Assess the morphology of the red blood cells.
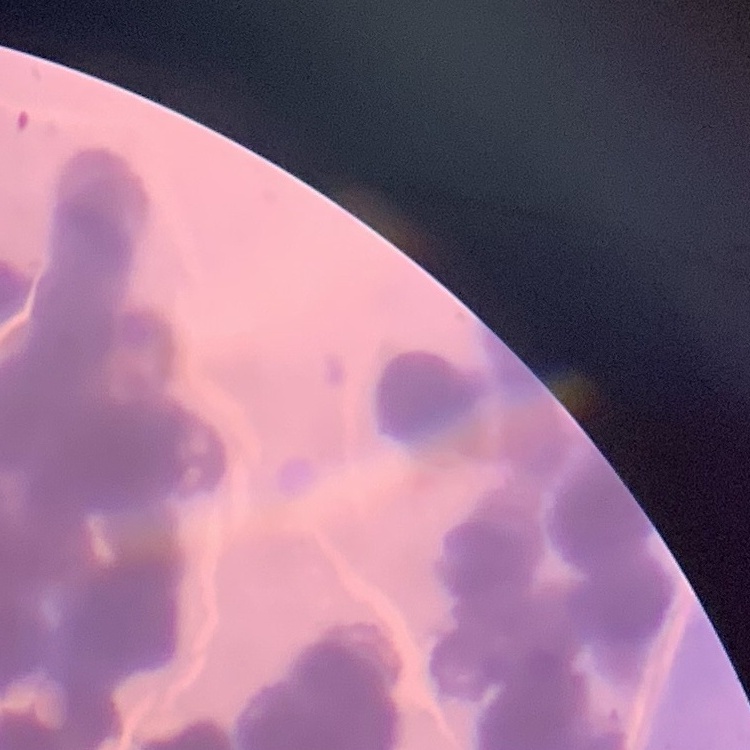

Rouleaux formation.

Summary:
  - Image type: one tile cut from a larger photomicrograph
  - Stain: Field's or Giemsa
  - Preparation: thin blood film